Classify this cell by malaria status.
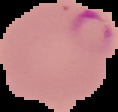
Parasitized.

Segmented cell region on a black background. Image is 118×112 pixels. From a thin blood film.